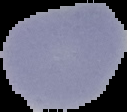
From a thin blood smear. Image is 127×112 pixels. Malaria status: uninfected. Cell region segmented out of the field of view; the surrounding area is masked to black.